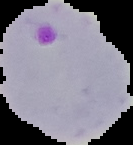

The area outside the segmented cell region is set to black. Result: malaria parasites detected. From a thin blood smear. Image is 133×145 pixels.